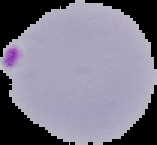
preparation = thin blood smear
image size = 157×145 pixels
image type = cell region segmented out of the field of view; surrounding area masked to black
result = Plasmodium parasites identified